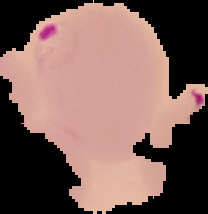

Summary:
  - Image type: segmented cell region on a black background
  - Result: malaria parasites identified
  - Preparation: thin blood smear
  - Image size: 208×214 pixels